Outline each blood parasite and name the species.
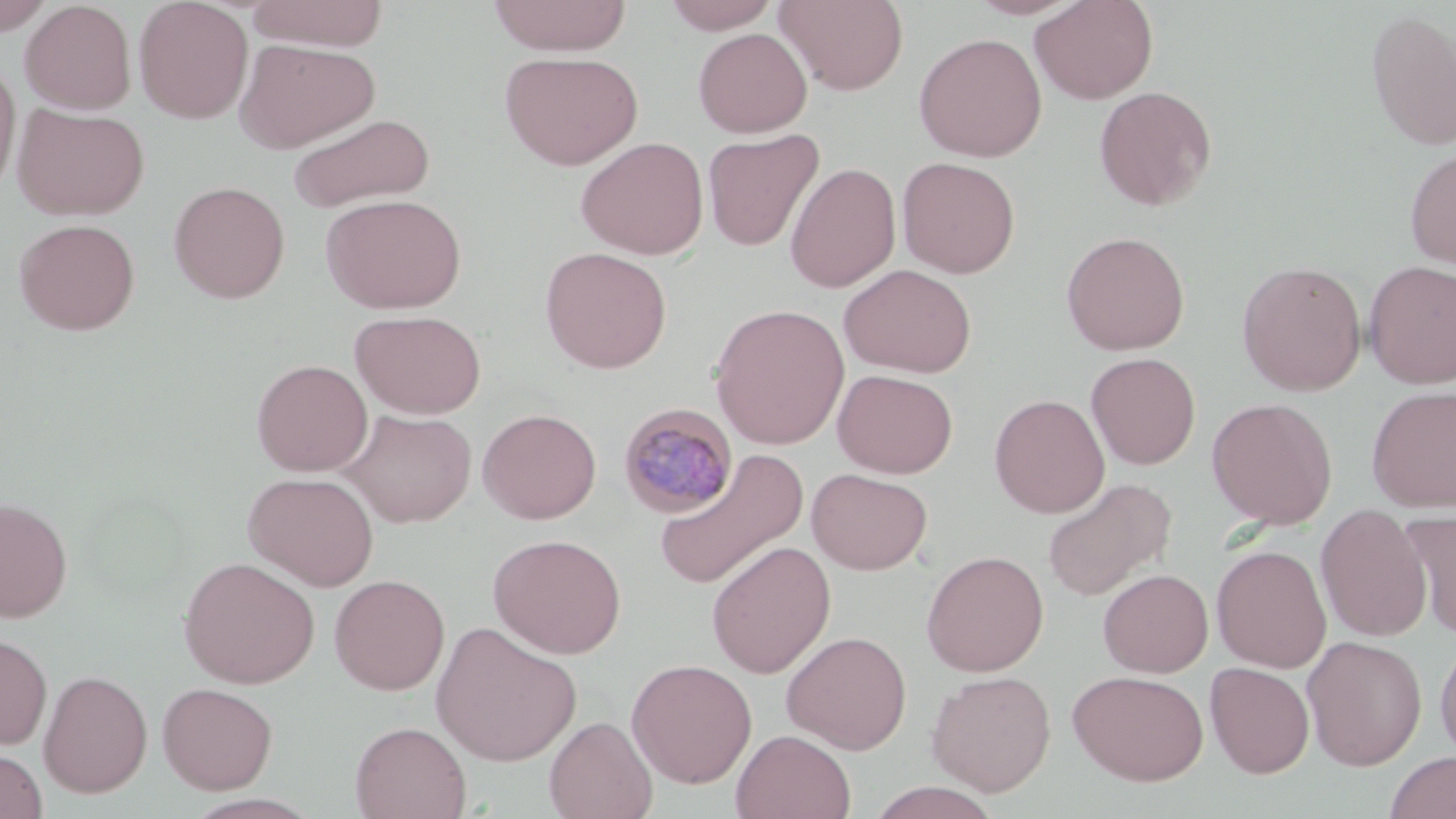
Approximate bounding boxes as named x1/y1/x2/y2 corners in pixels.
Plasmodium malariae-infected red blood cells: (x1=618, y1=402, x2=738, y2=518).
No Plasmodium falciparum, Plasmodium ovale, Plasmodium vivax, Babesia divergens, or Trypanosoma brucei observed.

Uninfected red blood cell locations: (x1=133, y1=0, x2=253, y2=124), (x1=247, y1=0, x2=389, y2=51), (x1=488, y1=0, x2=633, y2=56), (x1=774, y1=0, x2=910, y2=96), (x1=966, y1=0, x2=1088, y2=20), (x1=1029, y1=0, x2=1158, y2=104), (x1=20, y1=1, x2=136, y2=114), (x1=661, y1=1, x2=783, y2=34), (x1=0, y1=2, x2=55, y2=36), (x1=1365, y1=9, x2=1456, y2=151), (x1=693, y1=28, x2=812, y2=137), (x1=913, y1=32, x2=1048, y2=162), (x1=235, y1=38, x2=380, y2=153), (x1=499, y1=51, x2=643, y2=170), (x1=0, y1=56, x2=20, y2=202), (x1=1094, y1=86, x2=1217, y2=211), (x1=12, y1=104, x2=149, y2=220), (x1=286, y1=112, x2=436, y2=214), (x1=702, y1=128, x2=826, y2=252), (x1=575, y1=136, x2=709, y2=260), (x1=1405, y1=148, x2=1456, y2=270), (x1=897, y1=156, x2=1020, y2=278), (x1=785, y1=162, x2=901, y2=293), (x1=169, y1=181, x2=290, y2=303), (x1=321, y1=193, x2=467, y2=314), (x1=13, y1=218, x2=140, y2=335), (x1=1061, y1=230, x2=1190, y2=355), (x1=539, y1=246, x2=673, y2=374), (x1=1363, y1=260, x2=1456, y2=388), (x1=1237, y1=261, x2=1367, y2=395), (x1=839, y1=264, x2=977, y2=377), (x1=710, y1=303, x2=850, y2=450), (x1=350, y1=309, x2=486, y2=419), (x1=1085, y1=352, x2=1201, y2=470), (x1=251, y1=359, x2=373, y2=476), (x1=832, y1=368, x2=958, y2=478), (x1=1365, y1=385, x2=1456, y2=512), (x1=989, y1=393, x2=1109, y2=518), (x1=1207, y1=397, x2=1338, y2=528), (x1=478, y1=408, x2=602, y2=524), (x1=341, y1=409, x2=477, y2=527), (x1=652, y1=448, x2=810, y2=592), (x1=807, y1=468, x2=933, y2=575), (x1=243, y1=471, x2=379, y2=591), (x1=1041, y1=477, x2=1176, y2=603), (x1=0, y1=496, x2=73, y2=622), (x1=1316, y1=503, x2=1432, y2=643), (x1=1396, y1=510, x2=1456, y2=639), (x1=488, y1=533, x2=627, y2=658), (x1=706, y1=541, x2=836, y2=679), (x1=1212, y1=544, x2=1331, y2=672), (x1=921, y1=550, x2=1049, y2=676), (x1=178, y1=556, x2=319, y2=688), (x1=1098, y1=568, x2=1213, y2=677), (x1=329, y1=574, x2=450, y2=695), (x1=431, y1=621, x2=582, y2=766), (x1=781, y1=630, x2=912, y2=754), (x1=0, y1=631, x2=53, y2=750), (x1=1302, y1=635, x2=1427, y2=771), (x1=1435, y1=635, x2=1456, y2=763), (x1=626, y1=658, x2=757, y2=788), (x1=1205, y1=662, x2=1314, y2=778), (x1=39, y1=669, x2=153, y2=798), (x1=926, y1=670, x2=1056, y2=796), (x1=1068, y1=670, x2=1210, y2=785), (x1=157, y1=682, x2=277, y2=794), (x1=544, y1=716, x2=657, y2=819), (x1=350, y1=721, x2=471, y2=819), (x1=731, y1=729, x2=856, y2=818), (x1=1, y1=747, x2=48, y2=819), (x1=1383, y1=751, x2=1455, y2=819), (x1=866, y1=781, x2=1003, y2=819). Slide-level diagnosis: Plasmodium malariae. May-Grünwald-Giemsa-stained preparation. 1000x magnification. Image is 1456×819 pixels. Thin blood smear. One field of a larger specimen. Light microscopy.